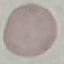

{
  "malaria_status": "uninfected",
  "preparation": "thin smear",
  "stain": "Giemsa",
  "capture": "smartphone through the microscope eyepiece",
  "image_type": "cell patch, automatically extracted from a larger field of view and resized to 64 × 64 pixels"
}